Report the malaria status of this cell.
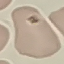

Uninfected.

preparation = thin blood smear
capture = smartphone camera at the microscope eyepiece
image type = automatically extracted cell patch, resized to 64 × 64 pixels
stain = Giemsa